Assess this cell for malaria.
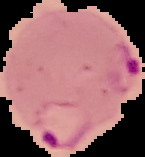

It is parasitized.

Summary:
  - Image type: segmented cell region with the area outside set to black
  - Image size: 145×157 pixels
  - Preparation: thin blood smear